Report the malaria status of this cell.
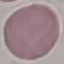

Uninfected.

Summary:
  - Image type: cell patch, automatically extracted from a larger field of view and resized to 64 × 64 pixels
  - Preparation: thin blood film
  - Capture: smartphone camera at the microscope eyepiece
  - Stain: Giemsa